Describe the morphology of the red blood cells.
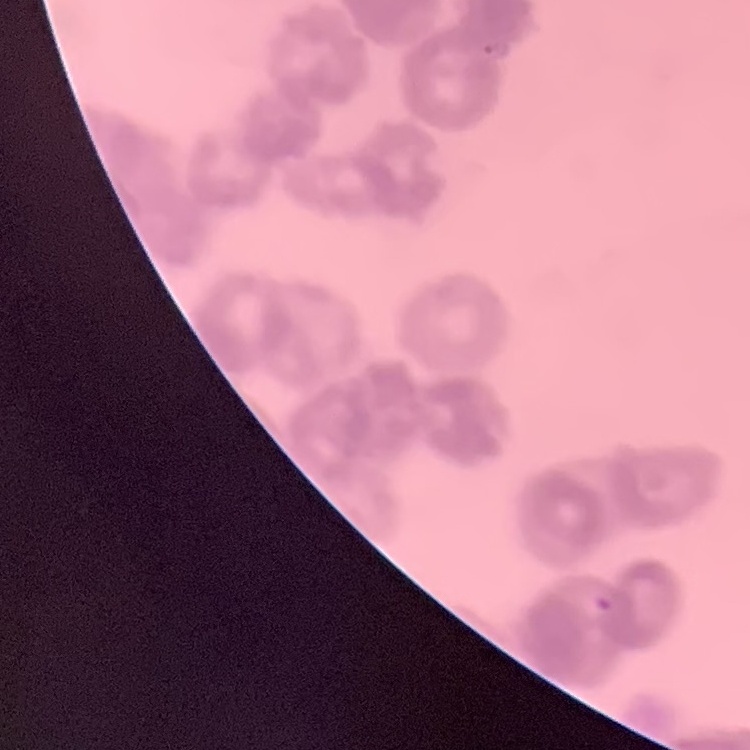

Rouleaux formation.

{
  "stain": "Field's or Giemsa",
  "preparation": "thin blood smear",
  "image_type": "one tile cut from a larger photomicrograph"
}